Report the malaria status of this cell.
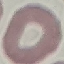
It is uninfected.

preparation = thin blood smear
image type = cell patch, automatically extracted from a larger field of view and resized to 64 × 64 pixels
capture = smartphone through the microscope eyepiece
stain = Giemsa